Find the red blood cells that are infected with Plasmodium falciparum, and any of indeterminate infection status.
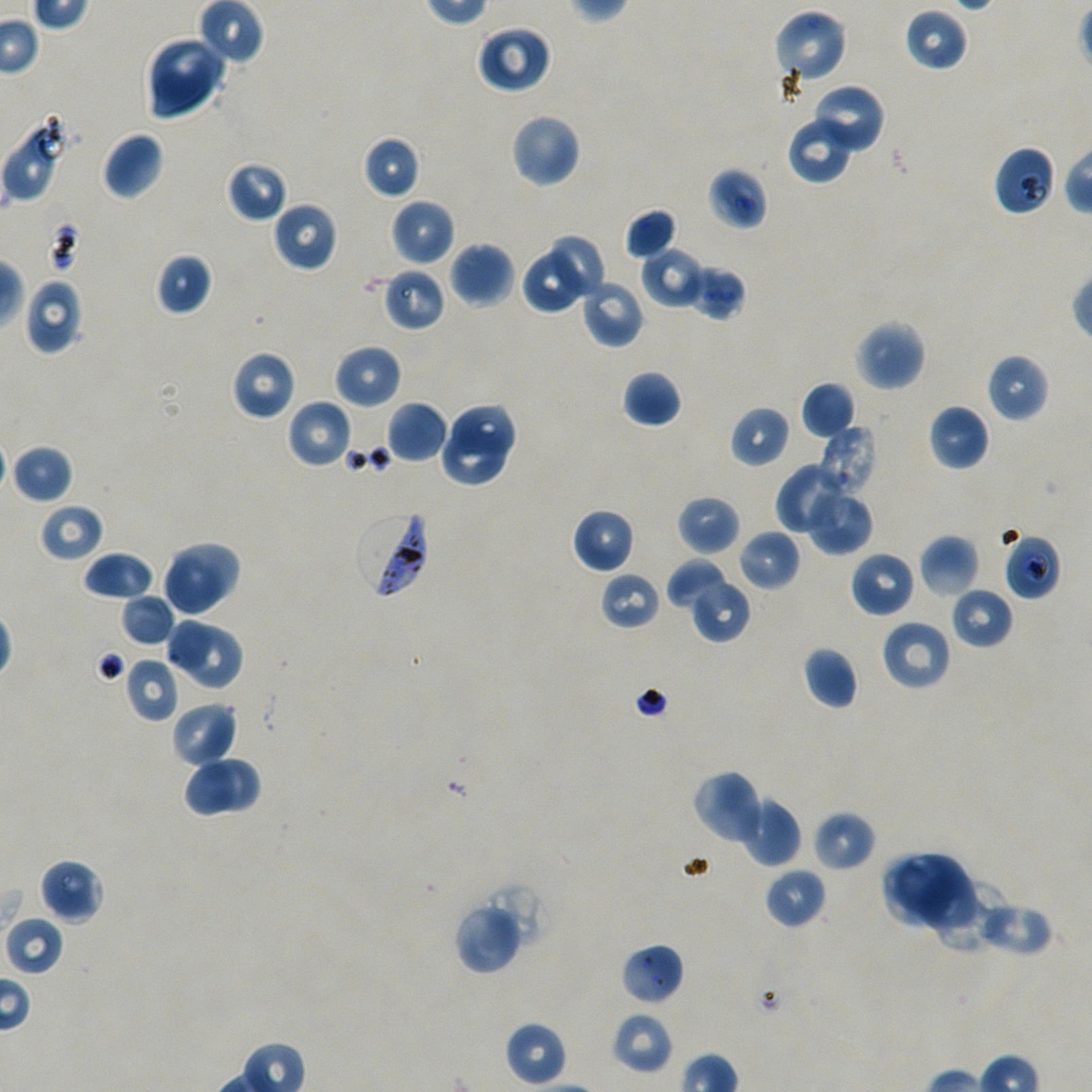
Approximate bounding boxes as [x1, y1, x2, y2] in pixels. Not every red blood cell is marked.
Infected red blood cells: [354, 509, 431, 600].
Red blood cells of indeterminate infection status: [1, 115, 68, 203], [994, 145, 1056, 217], [708, 167, 767, 230], [382, 268, 445, 332], [1003, 532, 1062, 600], [3, 914, 65, 977].

Summary:
  - Locations of uninfected red blood cells: [198, 0, 265, 66], [905, 7, 968, 72], [773, 9, 848, 88], [476, 25, 552, 94], [145, 35, 227, 120], [809, 84, 885, 156], [510, 113, 581, 187], [787, 116, 856, 185], [102, 132, 164, 201], [362, 136, 420, 200], [227, 161, 289, 223], [390, 198, 455, 266], [272, 200, 338, 272], [623, 208, 678, 261], [551, 232, 605, 298], [448, 241, 515, 308], [641, 248, 704, 308], [521, 252, 582, 315], [155, 253, 212, 316], [685, 264, 746, 322], [23, 278, 85, 355], [579, 278, 644, 348], [854, 319, 926, 391], [333, 344, 402, 409], [230, 350, 297, 421], [986, 353, 1050, 422], [622, 369, 682, 429], [801, 382, 856, 440], [286, 399, 353, 469], [386, 401, 449, 463], [452, 401, 517, 456], [928, 404, 989, 471], [729, 405, 790, 467], [438, 424, 509, 489], [820, 425, 877, 494], [10, 443, 73, 505], [776, 462, 842, 536], [805, 486, 874, 555], [676, 494, 740, 555], [39, 503, 105, 562], [571, 508, 636, 575], [737, 529, 801, 592], [919, 534, 979, 597], [168, 541, 242, 606], [83, 549, 154, 602], [850, 550, 917, 618], [161, 551, 227, 617], [667, 558, 731, 612], [599, 570, 661, 630], [689, 579, 750, 642], [949, 586, 1014, 650], [120, 594, 176, 647], [164, 617, 213, 668], [879, 619, 951, 691], [179, 623, 242, 689], [802, 647, 858, 710], [125, 658, 180, 723], [170, 702, 237, 769], [205, 757, 260, 812], [181, 759, 235, 819], [691, 769, 765, 846], [737, 794, 801, 867], [811, 810, 877, 872], [882, 852, 977, 933], [39, 858, 105, 924], [763, 867, 827, 928], [930, 877, 1001, 953], [483, 879, 551, 954], [453, 901, 524, 976], [976, 901, 1053, 955], [621, 943, 684, 1006], [611, 1011, 674, 1074], [505, 1021, 568, 1085]
  - Donor blood group: A+/O+
  - Preparation: thin blood film
  - Stain: Giemsa
  - Objective: 100x, oil immersion, numerical aperture 1.45
  - Image size: 1092×1092 pixels
  - Field of view: single
  - Culture: static in-vitro Plasmodium falciparum strain NF54